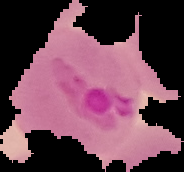

preparation = thin blood smear
image size = 184×172 pixels
image type = segmented cell region with the area outside set to black
result = malaria parasites detected